Identify the parasite.
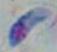

This is Toxoplasma gondii.

Summary:
  - Magnification: 1000x
  - Modality: micrograph